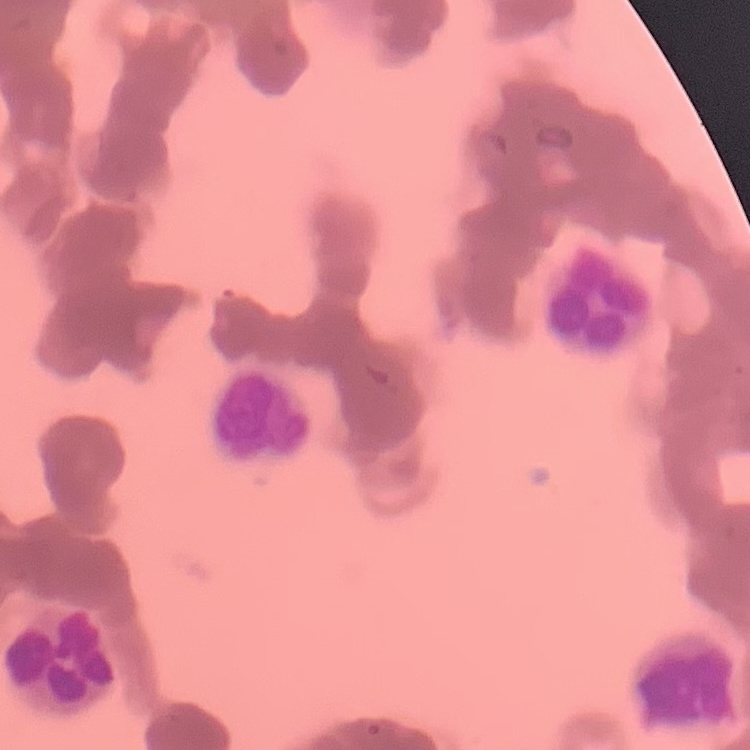

Summary:
  - Erythrocyte morphology: rouleaux formation
  - Image type: one tile cut from a larger photomicrograph
  - Stain: Field's or Giemsa
  - Preparation: thin peripheral smear